Describe the morphology of the red blood cells.
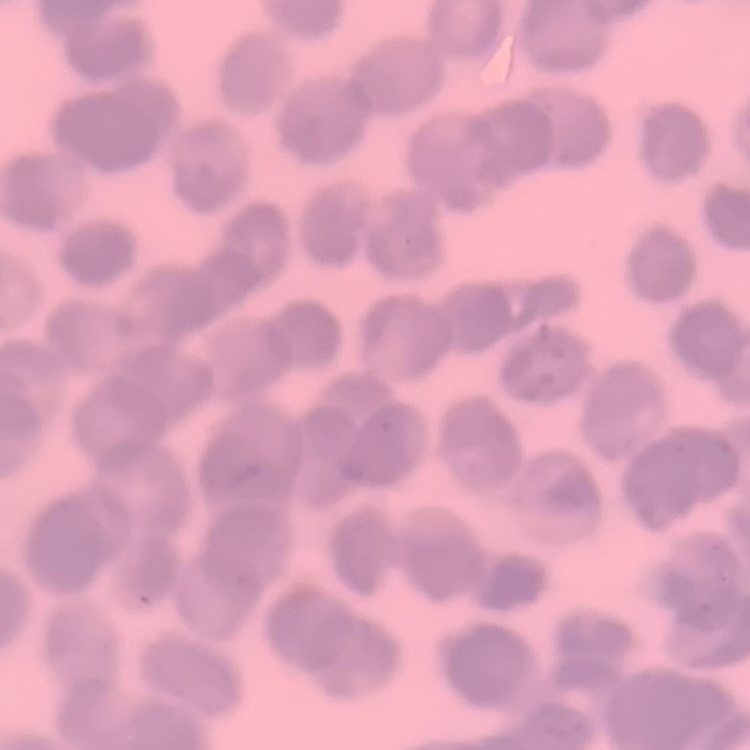
Rouleaux formation.

Summary:
  - Preparation: thin blood film
  - Stain: Field's or Giemsa
  - Image type: square crop of a larger photomicrograph